Outline platelets.
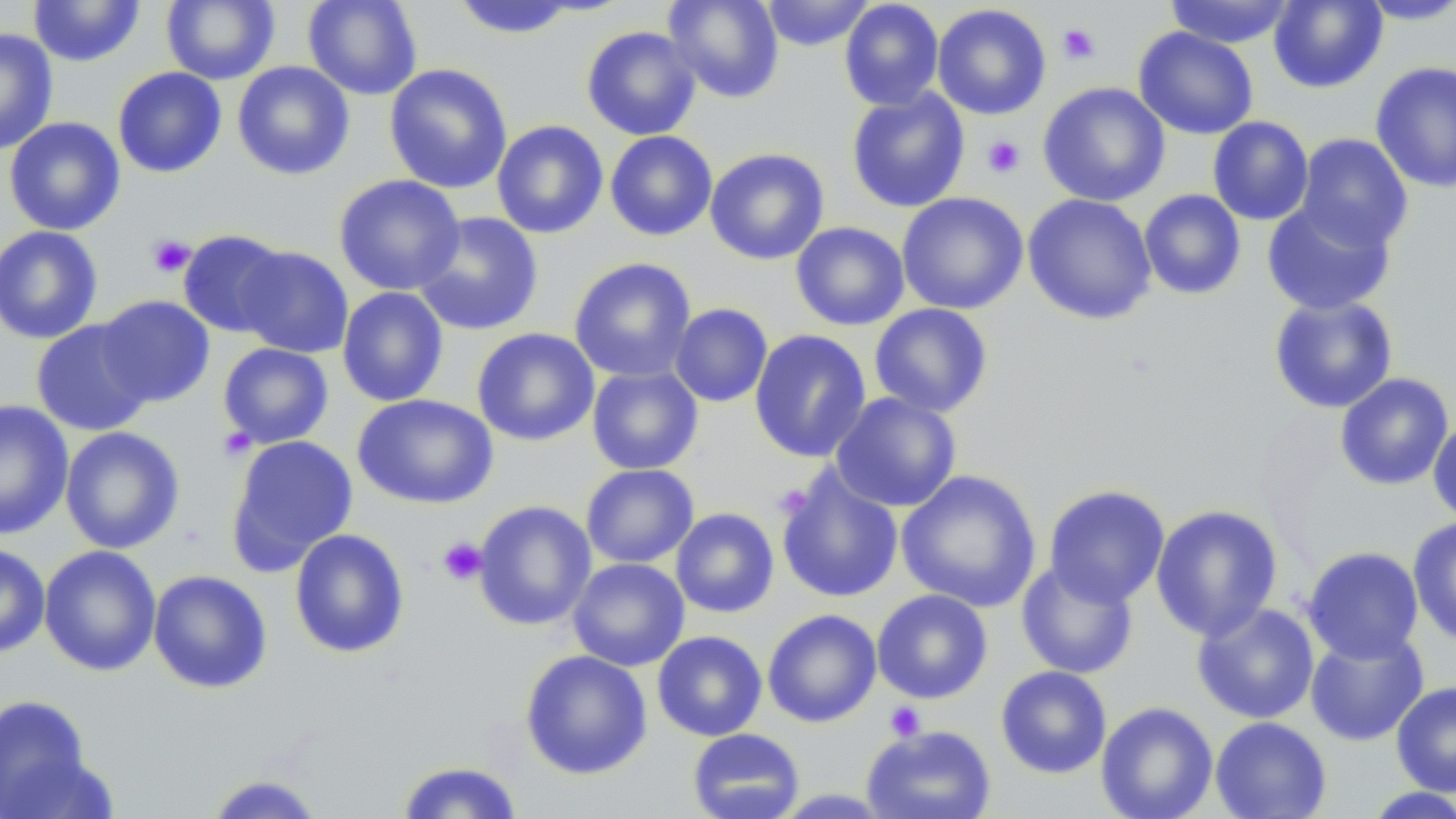
Approximate bounding boxes as named x1/y1/x2/y2 corners in pixels.
Platelets: (x1=1057, y1=23, x2=1101, y2=65), (x1=981, y1=135, x2=1026, y2=179), (x1=147, y1=234, x2=196, y2=278), (x1=218, y1=426, x2=255, y2=461), (x1=437, y1=537, x2=487, y2=586), (x1=884, y1=702, x2=925, y2=741).

Summary:
  - Uninfected red blood cell locations: (x1=29, y1=0, x2=145, y2=67), (x1=161, y1=0, x2=280, y2=85), (x1=303, y1=0, x2=422, y2=100), (x1=663, y1=0, x2=784, y2=104), (x1=761, y1=0, x2=875, y2=51), (x1=839, y1=0, x2=944, y2=111), (x1=1163, y1=0, x2=1298, y2=48), (x1=1268, y1=0, x2=1388, y2=93), (x1=450, y1=1, x2=579, y2=39), (x1=1356, y1=1, x2=1456, y2=25), (x1=932, y1=4, x2=1051, y2=120), (x1=581, y1=25, x2=701, y2=141), (x1=1133, y1=27, x2=1259, y2=140), (x1=1, y1=28, x2=58, y2=155), (x1=232, y1=61, x2=355, y2=180), (x1=1370, y1=61, x2=1456, y2=193), (x1=384, y1=63, x2=513, y2=194), (x1=112, y1=67, x2=227, y2=178), (x1=1037, y1=82, x2=1171, y2=207), (x1=846, y1=88, x2=970, y2=212), (x1=1208, y1=116, x2=1313, y2=225), (x1=4, y1=117, x2=125, y2=236), (x1=491, y1=120, x2=608, y2=239), (x1=605, y1=130, x2=718, y2=242), (x1=1295, y1=133, x2=1414, y2=252), (x1=704, y1=148, x2=829, y2=265), (x1=333, y1=174, x2=465, y2=296), (x1=1139, y1=189, x2=1246, y2=300), (x1=896, y1=192, x2=1029, y2=315), (x1=1022, y1=193, x2=1157, y2=325), (x1=1262, y1=199, x2=1396, y2=316), (x1=413, y1=212, x2=544, y2=336), (x1=791, y1=221, x2=910, y2=331), (x1=0, y1=225, x2=103, y2=345), (x1=177, y1=230, x2=290, y2=338), (x1=235, y1=245, x2=354, y2=358), (x1=569, y1=257, x2=696, y2=382), (x1=337, y1=286, x2=449, y2=407), (x1=96, y1=295, x2=216, y2=407), (x1=1268, y1=295, x2=1399, y2=414), (x1=670, y1=303, x2=772, y2=407), (x1=869, y1=303, x2=994, y2=418), (x1=31, y1=319, x2=155, y2=436), (x1=471, y1=327, x2=600, y2=446), (x1=749, y1=329, x2=871, y2=463), (x1=218, y1=343, x2=334, y2=449), (x1=587, y1=366, x2=703, y2=475), (x1=1334, y1=373, x2=1454, y2=491), (x1=831, y1=392, x2=962, y2=512), (x1=352, y1=394, x2=498, y2=510), (x1=0, y1=399, x2=74, y2=540), (x1=1428, y1=415, x2=1456, y2=526), (x1=60, y1=427, x2=185, y2=554), (x1=227, y1=434, x2=358, y2=569), (x1=581, y1=463, x2=699, y2=568), (x1=776, y1=467, x2=904, y2=603), (x1=896, y1=469, x2=1042, y2=612), (x1=1043, y1=485, x2=1170, y2=607), (x1=472, y1=500, x2=596, y2=631), (x1=1151, y1=504, x2=1283, y2=640), (x1=670, y1=508, x2=779, y2=618), (x1=1407, y1=517, x2=1456, y2=650), (x1=289, y1=528, x2=410, y2=659), (x1=0, y1=544, x2=50, y2=657), (x1=39, y1=545, x2=162, y2=676), (x1=1302, y1=546, x2=1424, y2=664), (x1=568, y1=557, x2=690, y2=671), (x1=1016, y1=559, x2=1139, y2=679), (x1=148, y1=569, x2=273, y2=693), (x1=872, y1=589, x2=993, y2=704), (x1=1192, y1=602, x2=1320, y2=724), (x1=762, y1=609, x2=882, y2=727), (x1=1305, y1=629, x2=1428, y2=746), (x1=652, y1=631, x2=768, y2=741), (x1=519, y1=649, x2=653, y2=779), (x1=996, y1=666, x2=1112, y2=778), (x1=1391, y1=680, x2=1456, y2=797), (x1=0, y1=695, x2=96, y2=817), (x1=1096, y1=701, x2=1218, y2=819), (x1=1210, y1=716, x2=1331, y2=818), (x1=862, y1=724, x2=997, y2=819), (x1=687, y1=728, x2=805, y2=819), (x1=394, y1=760, x2=525, y2=818), (x1=204, y1=773, x2=326, y2=818), (x1=1359, y1=787, x2=1456, y2=818)
  - Slide-level diagnosis: negative for blood parasites
  - Field of view: single
  - Modality: light microscopy
  - Preparation: thin blood smear
  - Image size: 1456×819 pixels
  - Stain: May-Grünwald-Giemsa
  - Magnification: 1000x